Describe the morphology of the red blood cells.
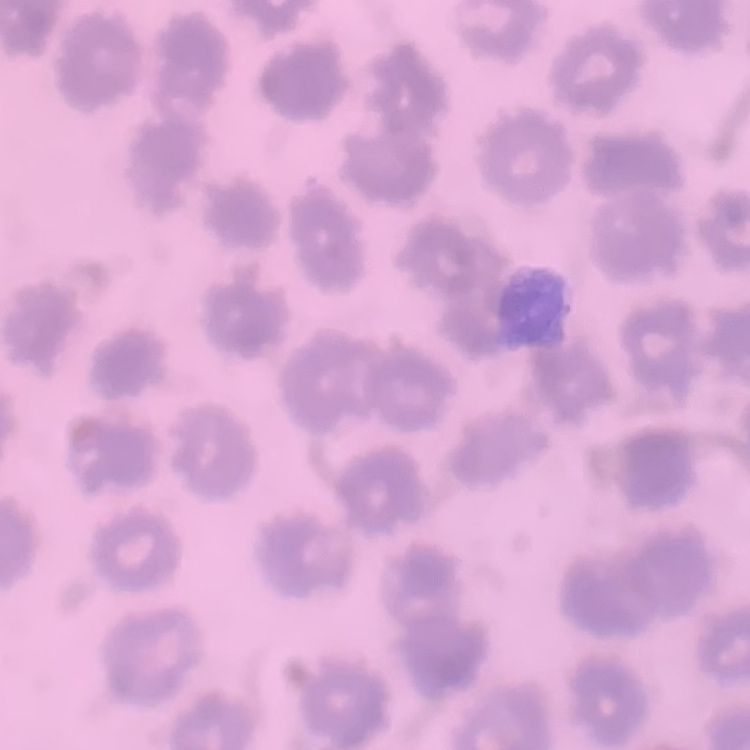
No rouleaux formation.

Summary:
  - Stain: Field's or Giemsa
  - Image type: square crop of a larger photomicrograph
  - Preparation: thin peripheral smear